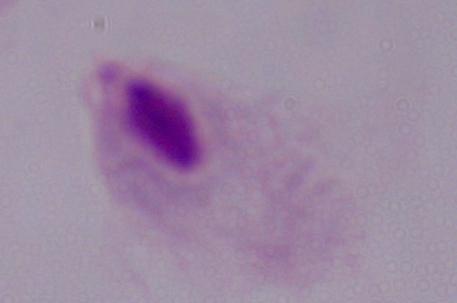

Summary:
  - Identification: trichomonad
  - Modality: photomicrograph
  - Magnification: 1000x